Identify the parasite.
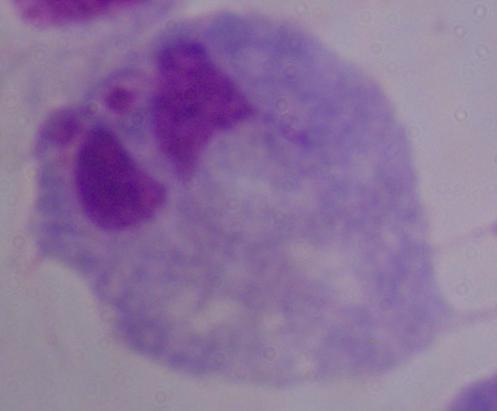

This is a trichomonad.

magnification = 1000x
modality = micrograph